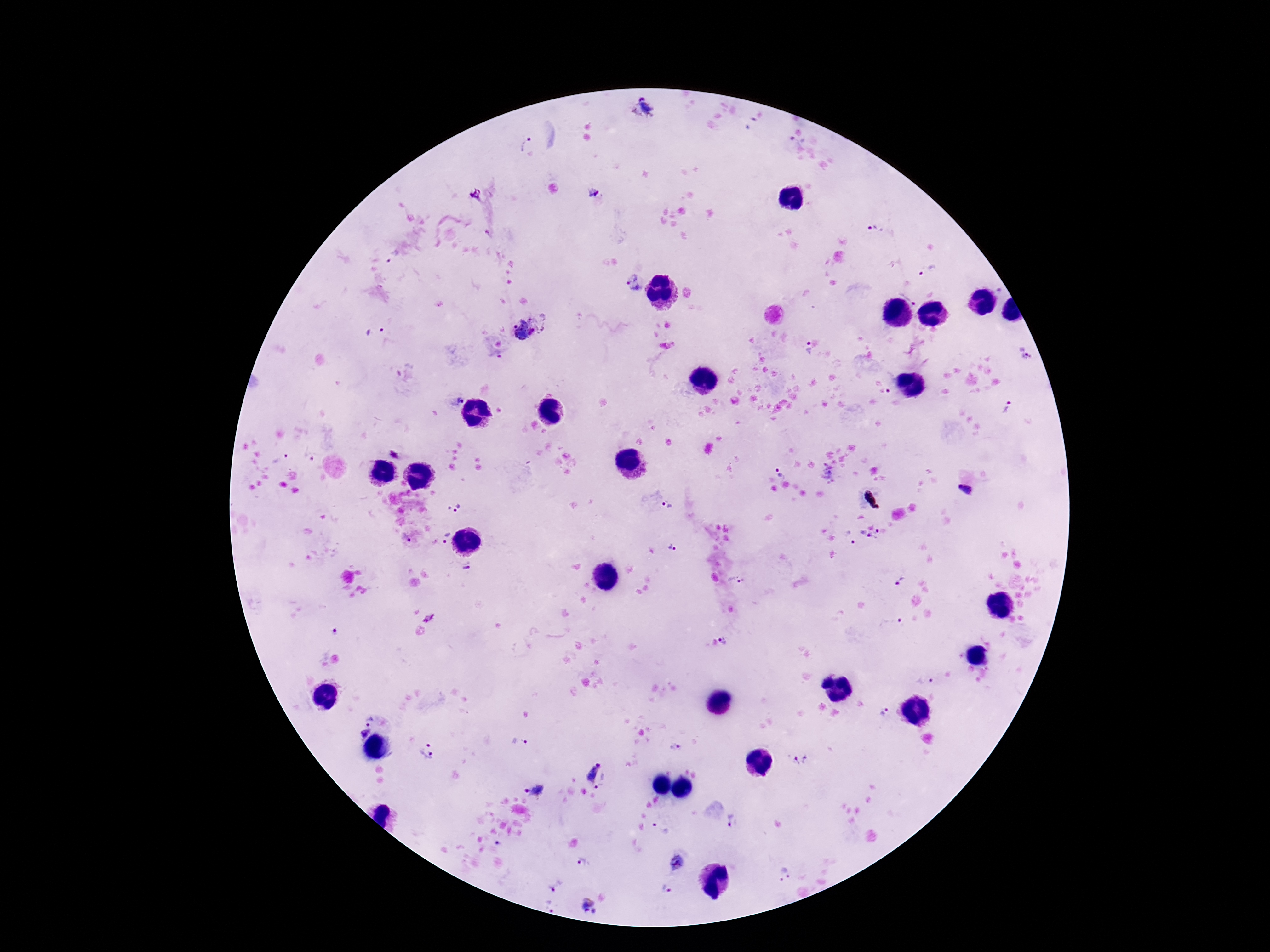

Approximate centers as [x, y] in pixels.
Summary:
  - Plasmodium parasite locations: [642, 108], [527, 144], [593, 190], [475, 196], [874, 230], [927, 269], [635, 284], [911, 291], [529, 325], [375, 332], [807, 349], [1027, 354], [889, 391], [455, 400], [1009, 408], [394, 450], [279, 459], [780, 472], [827, 475], [966, 491], [453, 507], [669, 507], [881, 533], [864, 535], [850, 537], [444, 538], [672, 547], [467, 567], [900, 578], [735, 580], [428, 620], [891, 622], [334, 631], [725, 640], [925, 680], [826, 681], [884, 714], [369, 718], [364, 735], [520, 742], [674, 747], [427, 752], [800, 759], [591, 768], [606, 782], [536, 790], [734, 821], [660, 828], [677, 862], [585, 863], [785, 873], [554, 886], [667, 889], [588, 905]
  - Patient malaria status: positive
  - Field of view: one from this slide
  - Capture: smartphone camera through the microscope eyepiece
  - Magnification: 100x
  - Stain: Giemsa
  - Preparation: thick blood film
  - Image size: 1270×952 pixels